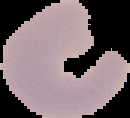
Summary:
  - Image size: 130×118 pixels
  - Image type: segmented cell region on a black background
  - Result: no Plasmodium parasites seen
  - Preparation: thin blood film